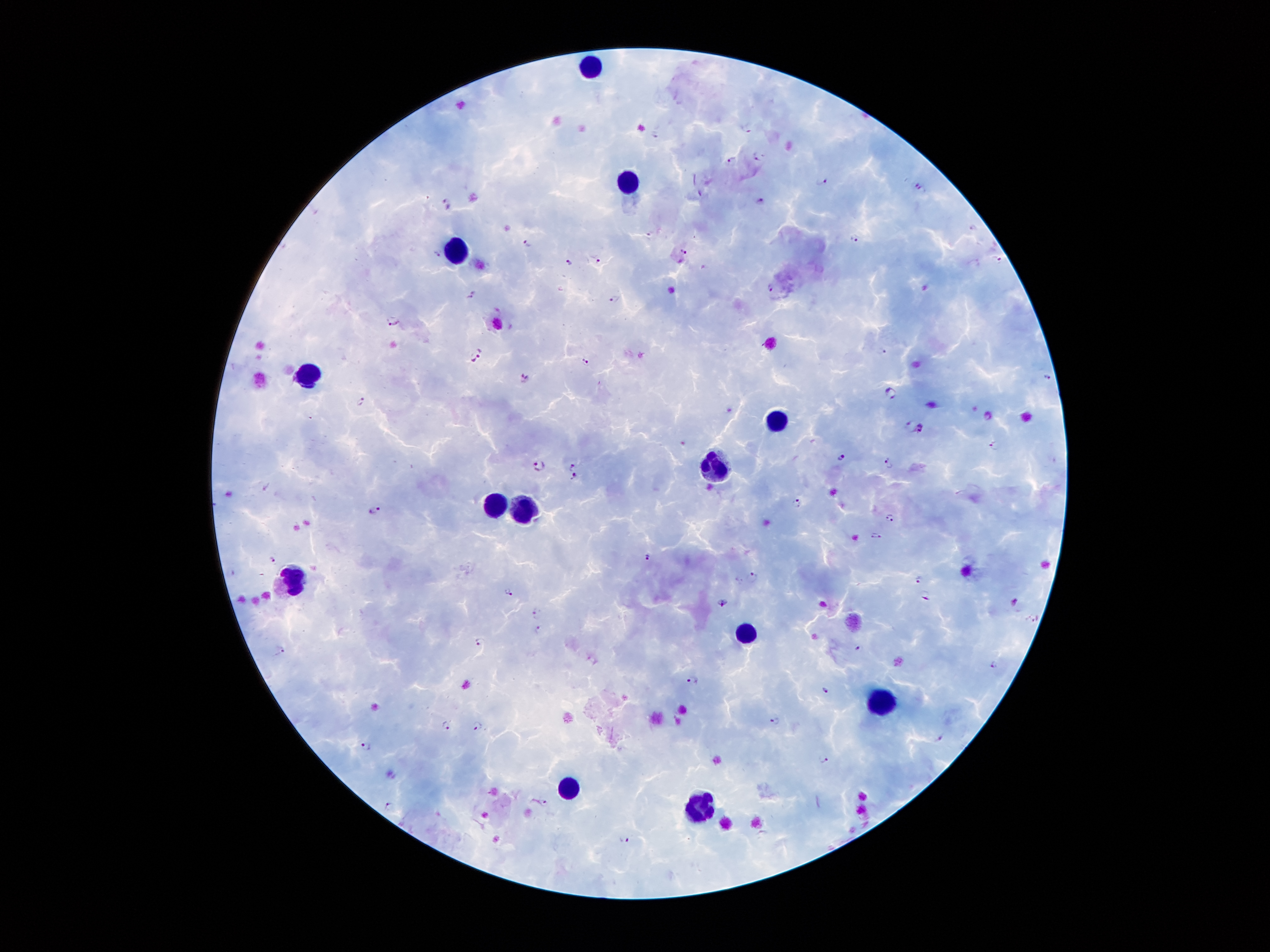
Approximate centers as [x, y] in pixels.
Summary:
  - Plasmodium parasite locations: [747, 126], [654, 133], [756, 154], [731, 160], [822, 180], [914, 183], [923, 190], [759, 201], [448, 204], [972, 228], [652, 235], [854, 237], [529, 244], [438, 251], [683, 252], [997, 260], [599, 262], [569, 263], [771, 287], [471, 295], [614, 299], [391, 320], [881, 350], [476, 354], [586, 359], [1046, 375], [523, 378], [889, 393], [362, 401], [909, 423], [919, 427], [995, 445], [840, 456], [889, 463], [538, 466], [573, 467], [576, 477], [796, 504], [376, 509], [891, 518], [876, 536], [648, 557], [272, 559], [754, 577], [919, 578], [508, 592], [923, 594], [1016, 602], [721, 603], [534, 613], [1033, 618], [539, 630], [480, 642], [860, 646], [280, 649], [993, 663], [694, 679], [824, 689], [777, 720], [478, 725], [446, 726], [938, 735], [364, 746], [823, 759], [546, 803], [390, 808], [624, 838]
  - Leukocyte locations: [591, 69], [628, 192], [455, 256], [309, 372], [775, 423], [716, 469], [494, 506], [523, 509], [296, 580], [744, 629], [882, 700], [573, 788], [699, 807]
  - Patient malaria status: positive for Plasmodium falciparum
  - Stain: Giemsa
  - Magnification: 100x
  - Preparation: thick blood film
  - Image size: 1270×952 pixels
  - Capture: smartphone camera through the microscope eyepiece
  - Field of view: one from this slide